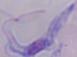

Summary:
  - Identification: trypanosome
  - Modality: photomicrograph
  - Magnification: 1000x